Classify this cell by malaria status.
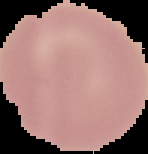
It is uninfected.

image_type: segmented cell region on a black background
preparation: thin blood film
image_size: 148×154 pixels